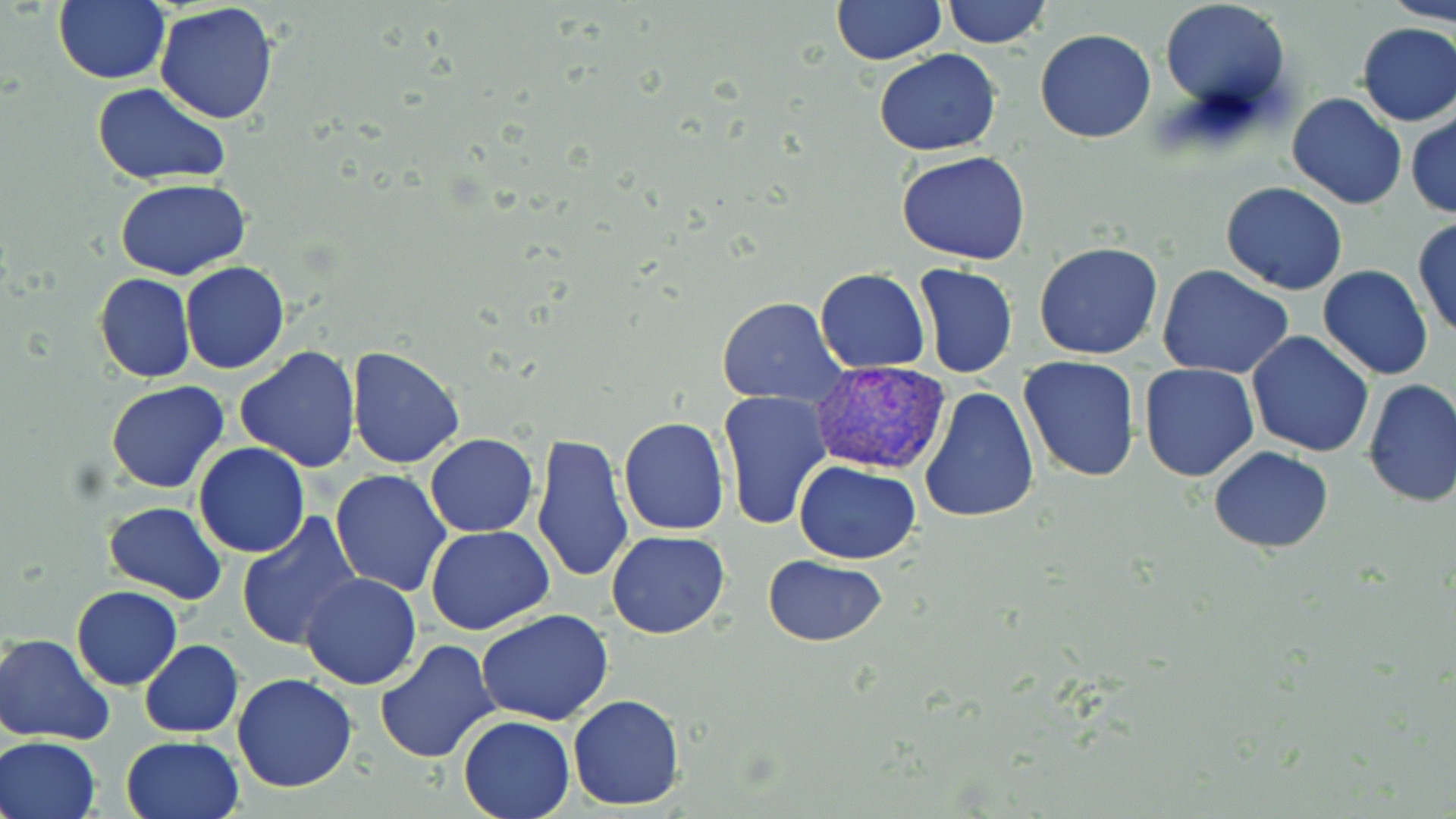
Summary:
  - Coordinate format: approximate bounding boxes as [x1, y1, x2, y2] in pixels
  - Plasmodium vivax-infected red blood cell locations: [812, 363, 953, 475]
  - Uninfected red blood cell locations: [54, 0, 171, 86], [942, 0, 1051, 48], [1385, 0, 1456, 24], [829, 1, 948, 64], [838, 1, 972, 114], [1158, 1, 1291, 117], [154, 3, 279, 125], [1354, 22, 1456, 127], [1035, 28, 1157, 144], [874, 50, 1001, 157], [91, 83, 232, 188], [1286, 90, 1407, 212], [1406, 111, 1456, 219], [897, 149, 1031, 266], [115, 178, 250, 279], [1220, 183, 1348, 295], [1412, 218, 1456, 339], [1034, 242, 1164, 361], [180, 261, 290, 375], [913, 263, 1018, 379], [1157, 265, 1295, 382], [1317, 265, 1434, 382], [815, 268, 929, 373], [94, 274, 196, 383], [718, 297, 847, 407], [1245, 331, 1376, 457], [234, 346, 362, 473], [347, 346, 464, 468], [1017, 355, 1142, 483], [1138, 364, 1259, 483], [1360, 379, 1456, 507], [106, 381, 230, 494], [919, 383, 1038, 525], [717, 390, 831, 530], [618, 417, 731, 536], [424, 433, 538, 537], [530, 433, 634, 584], [191, 442, 311, 558], [1208, 447, 1334, 552], [794, 460, 922, 564], [330, 468, 453, 597], [103, 502, 228, 603], [235, 511, 361, 650], [426, 526, 553, 636], [607, 529, 729, 639], [762, 556, 889, 647], [299, 573, 422, 692], [71, 585, 183, 690], [477, 609, 615, 726], [2, 633, 116, 745], [139, 640, 243, 737], [375, 640, 501, 763], [232, 674, 358, 793], [567, 694, 686, 809], [458, 714, 575, 818], [1, 735, 102, 819], [120, 736, 246, 819]
  - Slide-level diagnosis: Plasmodium vivax
  - Image size: 1456×819 pixels
  - Stain: May-Grünwald-Giemsa
  - Modality: optical microscopy
  - Preparation: thin blood smear
  - Field of view: one of a larger specimen
  - Magnification: 1000x